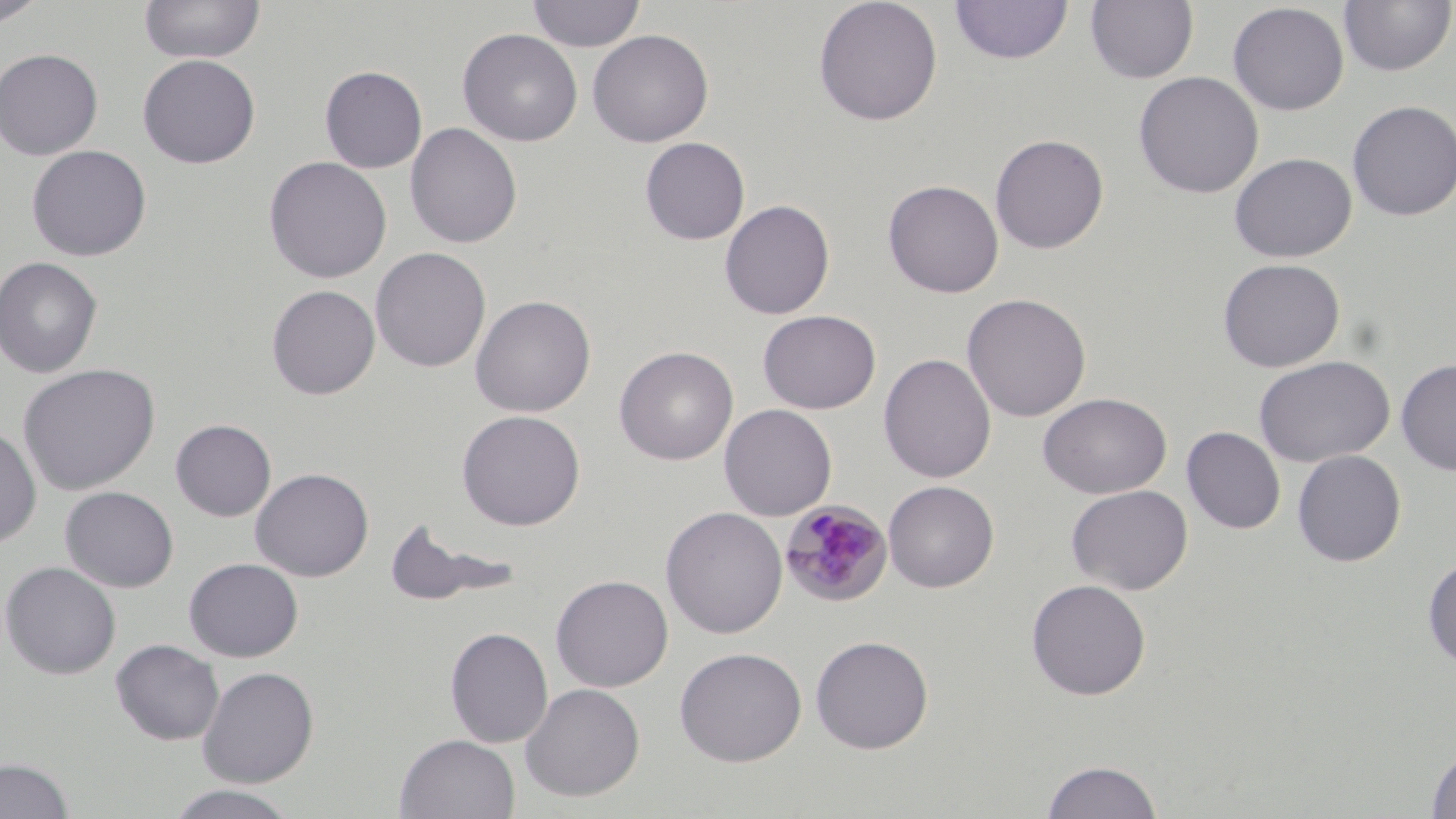
Approximate bounding boxes as named x1/y1/x2/y2 corners in pixels. Plasmodium malariae-infected red blood cell locations: (x1=779, y1=500, x2=892, y2=607). Uninfected red blood cell locations: (x1=1, y1=0, x2=46, y2=26), (x1=138, y1=0, x2=266, y2=64), (x1=527, y1=0, x2=646, y2=52), (x1=813, y1=0, x2=943, y2=126), (x1=1084, y1=0, x2=1200, y2=84), (x1=948, y1=1, x2=1074, y2=65), (x1=1338, y1=1, x2=1455, y2=77), (x1=1227, y1=3, x2=1349, y2=116), (x1=458, y1=28, x2=583, y2=147), (x1=587, y1=29, x2=714, y2=147), (x1=0, y1=48, x2=103, y2=160), (x1=137, y1=54, x2=260, y2=168), (x1=319, y1=65, x2=428, y2=173), (x1=1133, y1=71, x2=1264, y2=198), (x1=1347, y1=99, x2=1456, y2=221), (x1=405, y1=123, x2=522, y2=249), (x1=990, y1=134, x2=1109, y2=253), (x1=640, y1=136, x2=750, y2=245), (x1=26, y1=144, x2=152, y2=262), (x1=1228, y1=152, x2=1356, y2=263), (x1=263, y1=156, x2=392, y2=284), (x1=882, y1=179, x2=1004, y2=298), (x1=719, y1=199, x2=835, y2=320), (x1=370, y1=247, x2=491, y2=373), (x1=0, y1=256, x2=102, y2=378), (x1=1217, y1=258, x2=1345, y2=372), (x1=266, y1=284, x2=380, y2=399), (x1=961, y1=293, x2=1091, y2=421), (x1=470, y1=295, x2=596, y2=417), (x1=757, y1=309, x2=881, y2=414), (x1=614, y1=345, x2=738, y2=465), (x1=878, y1=353, x2=996, y2=483), (x1=1254, y1=355, x2=1395, y2=468), (x1=1396, y1=357, x2=1456, y2=476), (x1=18, y1=364, x2=160, y2=495), (x1=1038, y1=392, x2=1172, y2=499), (x1=719, y1=404, x2=837, y2=521), (x1=457, y1=409, x2=586, y2=531), (x1=170, y1=419, x2=276, y2=521), (x1=0, y1=425, x2=42, y2=549), (x1=1182, y1=426, x2=1285, y2=534), (x1=1292, y1=450, x2=1406, y2=567), (x1=250, y1=467, x2=374, y2=582), (x1=883, y1=480, x2=999, y2=592), (x1=1066, y1=484, x2=1193, y2=595), (x1=60, y1=486, x2=179, y2=592), (x1=661, y1=506, x2=787, y2=639), (x1=383, y1=516, x2=522, y2=608), (x1=1422, y1=554, x2=1456, y2=672), (x1=184, y1=558, x2=303, y2=662), (x1=1, y1=561, x2=121, y2=680), (x1=551, y1=574, x2=674, y2=692), (x1=1025, y1=578, x2=1151, y2=700), (x1=444, y1=626, x2=553, y2=747), (x1=810, y1=635, x2=934, y2=754), (x1=111, y1=639, x2=224, y2=745), (x1=674, y1=646, x2=807, y2=766), (x1=197, y1=665, x2=320, y2=788), (x1=520, y1=682, x2=645, y2=801), (x1=395, y1=733, x2=520, y2=819), (x1=1425, y1=743, x2=1456, y2=818), (x1=0, y1=757, x2=74, y2=818), (x1=1039, y1=759, x2=1164, y2=818), (x1=163, y1=784, x2=302, y2=819). Slide-level diagnosis: Plasmodium malariae. Light microscopy. Image is 1456×819 pixels. May-Grünwald-Giemsa stain. Single field of view. Thin blood smear. 1000x magnification.